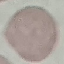
result = no malaria parasites seen
preparation = thin blood film
image type = automatically extracted cell patch, resized to 64 × 64 pixels
capture = smartphone through the microscope eyepiece
stain = Giemsa